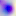
identification = Toxoplasma gondii
modality = micrograph
magnification = 400x